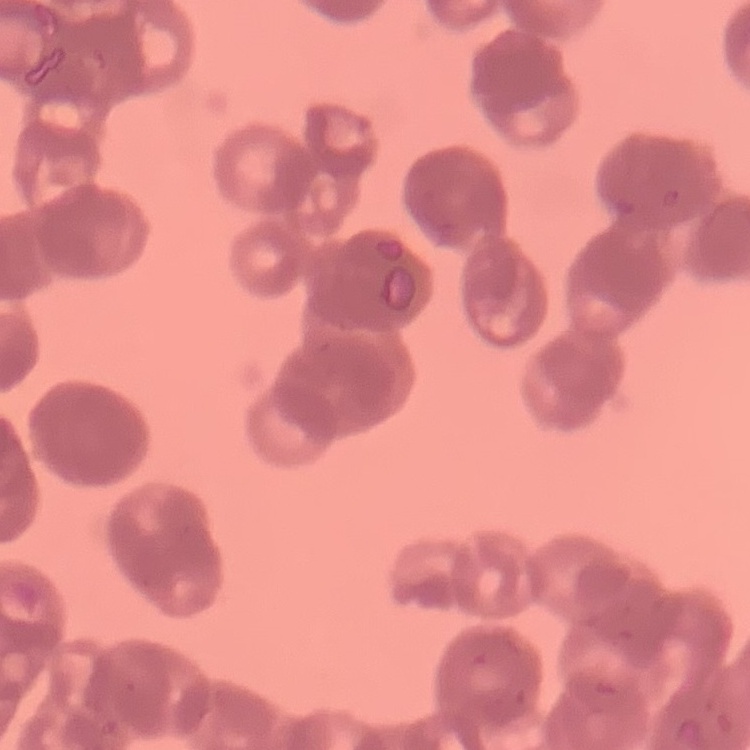

Summary:
  - Erythrocyte morphology: rouleaux formation
  - Image type: one tile cut from a larger photomicrograph
  - Stain: Field's or Giemsa
  - Preparation: thin peripheral smear